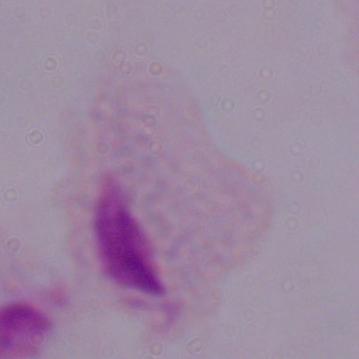 A trichomonad is shown. Micrograph. 1000x magnification.